Name the parasite shown.
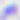
Toxoplasma gondii.

Photomicrograph. 400x magnification.